Outline each blood parasite and name the species.
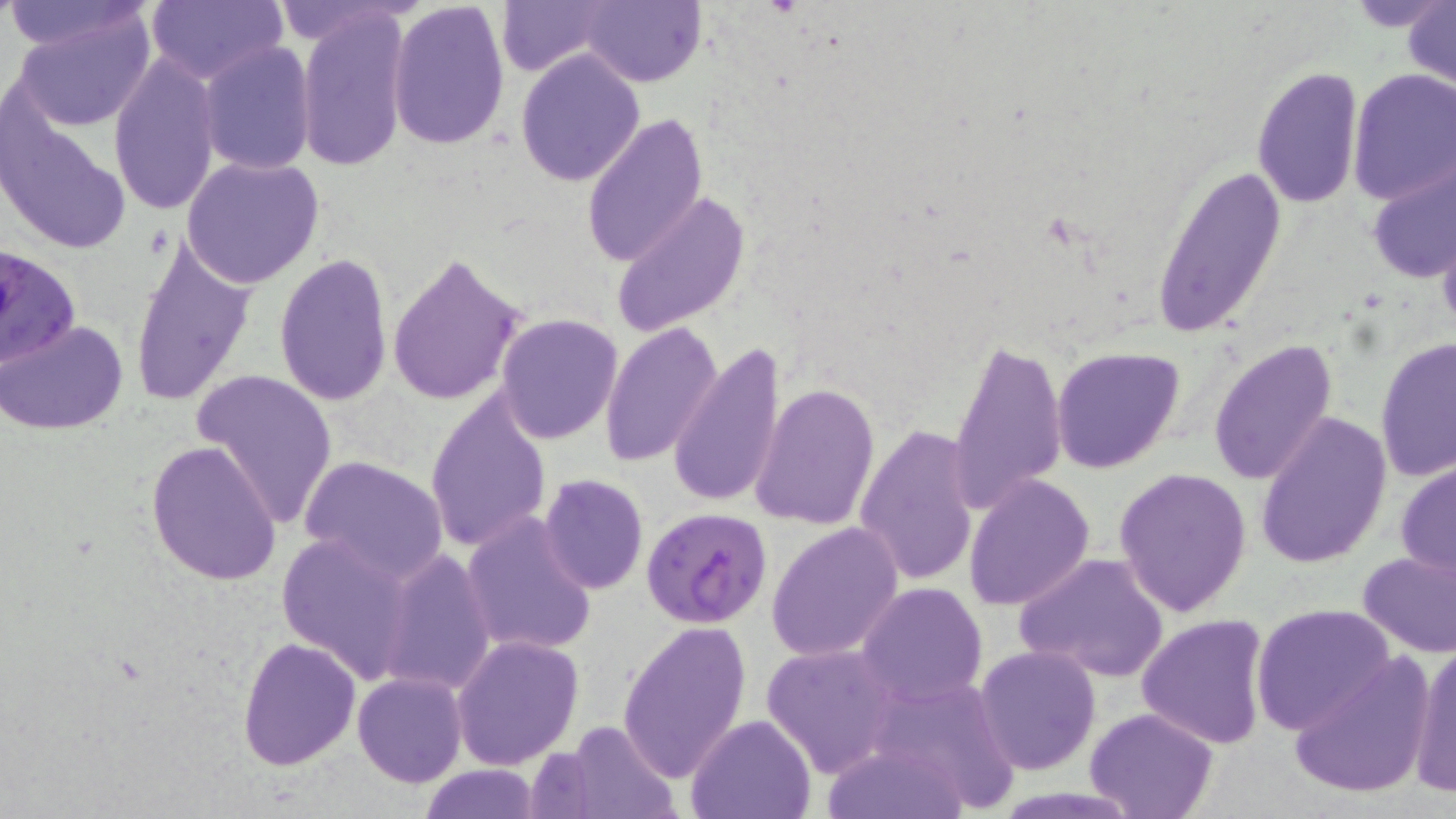
Approximate bounding boxes as named x1/y1/x2/y2 corners in pixels.
Plasmodium falciparum-infected red blood cells: (x1=0, y1=242, x2=80, y2=370), (x1=639, y1=506, x2=772, y2=629).
No Plasmodium ovale, Plasmodium malariae, Plasmodium vivax, Babesia divergens, or Trypanosoma brucei observed.

Uninfected red blood cell locations: (x1=0, y1=0, x2=160, y2=56), (x1=144, y1=0, x2=286, y2=85), (x1=386, y1=0, x2=511, y2=151), (x1=494, y1=0, x2=619, y2=77), (x1=580, y1=0, x2=706, y2=87), (x1=1403, y1=3, x2=1456, y2=91), (x1=297, y1=6, x2=413, y2=176), (x1=10, y1=10, x2=158, y2=129), (x1=200, y1=41, x2=315, y2=175), (x1=515, y1=48, x2=645, y2=187), (x1=107, y1=53, x2=222, y2=216), (x1=1250, y1=67, x2=1364, y2=210), (x1=1347, y1=70, x2=1456, y2=204), (x1=2, y1=110, x2=127, y2=254), (x1=583, y1=114, x2=708, y2=266), (x1=182, y1=155, x2=326, y2=290), (x1=1365, y1=158, x2=1456, y2=284), (x1=1150, y1=161, x2=1285, y2=339), (x1=613, y1=189, x2=752, y2=337), (x1=1436, y1=223, x2=1456, y2=339), (x1=128, y1=237, x2=254, y2=408), (x1=274, y1=250, x2=395, y2=407), (x1=386, y1=251, x2=528, y2=406), (x1=496, y1=313, x2=623, y2=443), (x1=2, y1=320, x2=127, y2=436), (x1=601, y1=321, x2=724, y2=469), (x1=1376, y1=335, x2=1455, y2=481), (x1=948, y1=336, x2=1067, y2=515), (x1=667, y1=340, x2=788, y2=509), (x1=1208, y1=340, x2=1338, y2=487), (x1=1050, y1=346, x2=1185, y2=474), (x1=191, y1=369, x2=338, y2=530), (x1=750, y1=381, x2=879, y2=529), (x1=424, y1=388, x2=549, y2=555), (x1=1253, y1=412, x2=1392, y2=569), (x1=854, y1=424, x2=982, y2=586), (x1=145, y1=440, x2=282, y2=585), (x1=299, y1=455, x2=448, y2=583), (x1=1395, y1=461, x2=1456, y2=578), (x1=1114, y1=468, x2=1253, y2=617), (x1=538, y1=474, x2=648, y2=593), (x1=963, y1=474, x2=1095, y2=612), (x1=461, y1=512, x2=598, y2=655), (x1=767, y1=521, x2=903, y2=662), (x1=274, y1=529, x2=418, y2=682), (x1=1356, y1=548, x2=1456, y2=657), (x1=378, y1=549, x2=497, y2=696), (x1=253, y1=550, x2=389, y2=754), (x1=1013, y1=551, x2=1169, y2=685), (x1=855, y1=581, x2=989, y2=707), (x1=1250, y1=603, x2=1396, y2=735), (x1=1136, y1=614, x2=1272, y2=749), (x1=616, y1=618, x2=752, y2=782), (x1=451, y1=635, x2=584, y2=770), (x1=237, y1=636, x2=362, y2=771), (x1=763, y1=643, x2=898, y2=777), (x1=974, y1=644, x2=1103, y2=775), (x1=1408, y1=644, x2=1456, y2=797), (x1=1287, y1=652, x2=1435, y2=801), (x1=354, y1=655, x2=570, y2=779), (x1=353, y1=671, x2=467, y2=787), (x1=864, y1=673, x2=1021, y2=811), (x1=1084, y1=706, x2=1220, y2=819), (x1=686, y1=714, x2=815, y2=819), (x1=562, y1=719, x2=681, y2=819), (x1=821, y1=738, x2=971, y2=818), (x1=414, y1=763, x2=544, y2=819). Slide-level diagnosis: Plasmodium falciparum. Light microscopy. 1000x magnification. Image is 1456×819 pixels. Single field of view. Thin blood film. May-Grünwald-Giemsa stain.